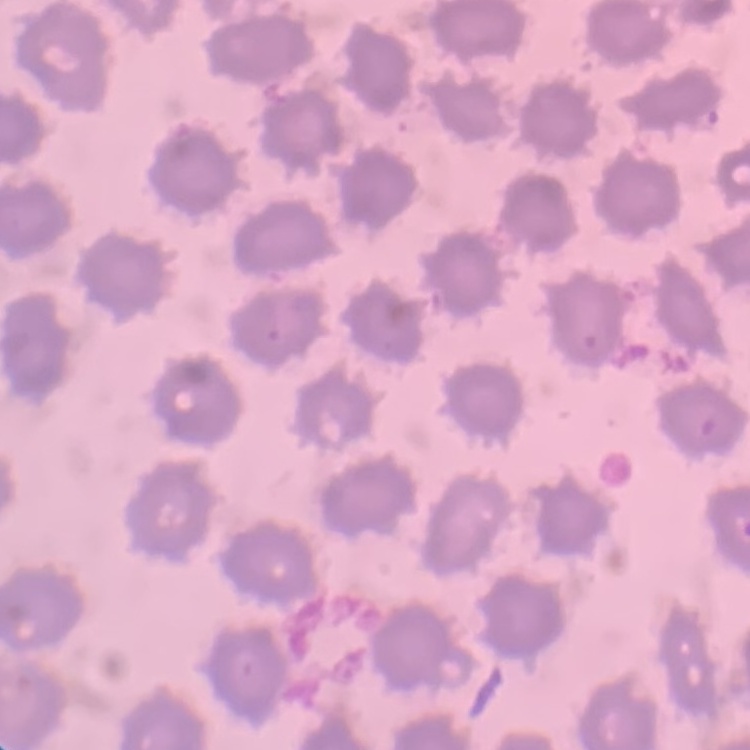 The red blood cells show no rouleaux formation. Field's or Giemsa stain. One tile cut from a larger photomicrograph. Thin blood film.